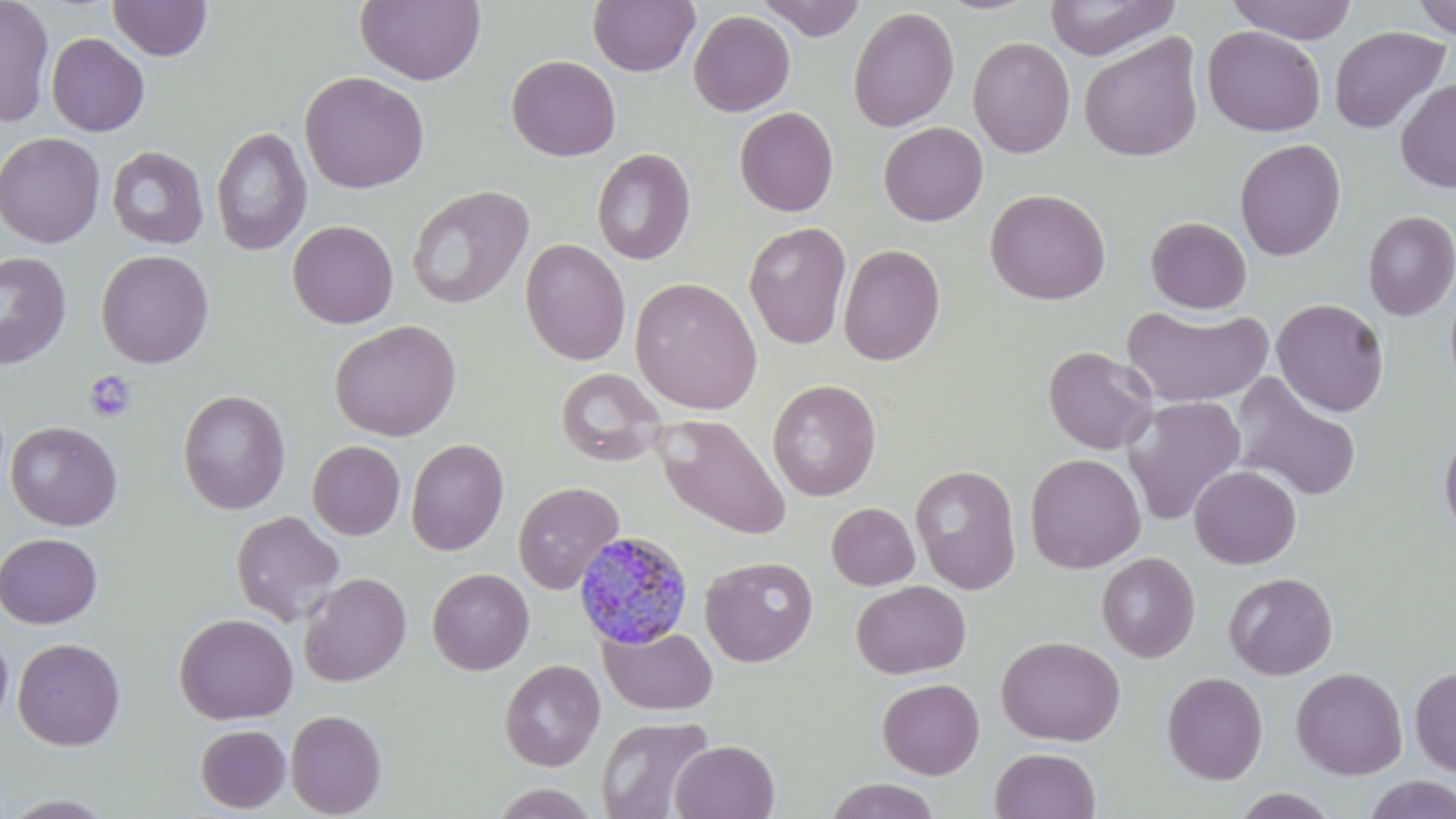
{
  "slide_level_diagnosis": "Plasmodium malariae",
  "modality": "optical microscopy",
  "stain": "May-Grünwald-Giemsa",
  "preparation": "thin blood film",
  "magnification": "1000x",
  "platelet_locations": "approximate bounding boxes as named x1/y1/x2/y2 corners in pixels: (x1=84, y1=370, x2=136, y2=423)",
  "image_size": "1456×819 pixels",
  "field_of_view": "one of a larger specimen",
  "uninfected_red_blood_cell_locations": "approximate bounding boxes as named x1/y1/x2/y2 corners in pixels: (x1=0, y1=0, x2=55, y2=128), (x1=108, y1=0, x2=212, y2=61), (x1=354, y1=0, x2=486, y2=85), (x1=587, y1=0, x2=700, y2=77), (x1=757, y1=0, x2=865, y2=41), (x1=1043, y1=0, x2=1180, y2=61), (x1=1226, y1=0, x2=1357, y2=44), (x1=1411, y1=0, x2=1456, y2=39), (x1=848, y1=6, x2=960, y2=132), (x1=688, y1=9, x2=796, y2=116), (x1=1202, y1=25, x2=1326, y2=137), (x1=1328, y1=25, x2=1451, y2=135), (x1=46, y1=32, x2=150, y2=137), (x1=1079, y1=33, x2=1204, y2=162), (x1=967, y1=36, x2=1076, y2=159), (x1=506, y1=55, x2=621, y2=161), (x1=299, y1=70, x2=429, y2=194), (x1=1395, y1=79, x2=1456, y2=193), (x1=734, y1=106, x2=839, y2=217), (x1=879, y1=122, x2=988, y2=225), (x1=211, y1=126, x2=312, y2=256), (x1=0, y1=132, x2=105, y2=248), (x1=1234, y1=138, x2=1346, y2=261), (x1=106, y1=145, x2=209, y2=249), (x1=591, y1=148, x2=696, y2=265), (x1=406, y1=184, x2=535, y2=310), (x1=985, y1=188, x2=1111, y2=305), (x1=1362, y1=210, x2=1456, y2=321), (x1=1145, y1=216, x2=1252, y2=314), (x1=287, y1=220, x2=399, y2=328), (x1=744, y1=221, x2=852, y2=349), (x1=519, y1=238, x2=631, y2=365), (x1=837, y1=244, x2=945, y2=365), (x1=96, y1=249, x2=214, y2=368), (x1=0, y1=250, x2=73, y2=369), (x1=629, y1=277, x2=763, y2=414), (x1=1444, y1=279, x2=1456, y2=395), (x1=1272, y1=298, x2=1389, y2=416), (x1=1121, y1=303, x2=1273, y2=408), (x1=329, y1=319, x2=462, y2=441), (x1=1042, y1=345, x2=1158, y2=455), (x1=555, y1=367, x2=667, y2=467), (x1=1229, y1=372, x2=1363, y2=502), (x1=767, y1=379, x2=882, y2=501), (x1=177, y1=389, x2=290, y2=514), (x1=1121, y1=396, x2=1247, y2=526), (x1=655, y1=416, x2=791, y2=540), (x1=5, y1=420, x2=123, y2=531), (x1=1439, y1=426, x2=1456, y2=542), (x1=405, y1=438, x2=509, y2=556), (x1=307, y1=440, x2=405, y2=540), (x1=1024, y1=453, x2=1146, y2=573), (x1=910, y1=464, x2=1021, y2=595), (x1=1189, y1=465, x2=1301, y2=569), (x1=513, y1=481, x2=624, y2=594), (x1=826, y1=502, x2=919, y2=590), (x1=230, y1=510, x2=345, y2=626), (x1=0, y1=532, x2=102, y2=627), (x1=1096, y1=552, x2=1200, y2=663), (x1=700, y1=556, x2=818, y2=668), (x1=427, y1=568, x2=534, y2=675), (x1=298, y1=572, x2=412, y2=687), (x1=1224, y1=572, x2=1338, y2=680), (x1=851, y1=580, x2=971, y2=679), (x1=174, y1=613, x2=298, y2=724), (x1=599, y1=625, x2=718, y2=715), (x1=0, y1=629, x2=14, y2=729), (x1=995, y1=635, x2=1125, y2=746), (x1=12, y1=638, x2=126, y2=751), (x1=499, y1=659, x2=605, y2=772), (x1=1409, y1=666, x2=1456, y2=777), (x1=1291, y1=667, x2=1408, y2=780), (x1=1161, y1=671, x2=1268, y2=785), (x1=877, y1=678, x2=985, y2=779), (x1=285, y1=709, x2=387, y2=818), (x1=596, y1=715, x2=716, y2=819), (x1=195, y1=724, x2=291, y2=813), (x1=671, y1=740, x2=780, y2=819), (x1=989, y1=747, x2=1101, y2=819), (x1=1363, y1=774, x2=1456, y2=819), (x1=821, y1=778, x2=942, y2=819), (x1=488, y1=783, x2=601, y2=819), (x1=1232, y1=788, x2=1342, y2=819)",
  "plasmodium_malariae_infected_red_blood_cell_locations": "approximate bounding boxes as named x1/y1/x2/y2 corners in pixels: (x1=573, y1=530, x2=694, y2=650)"
}